Outline every leukocyte.
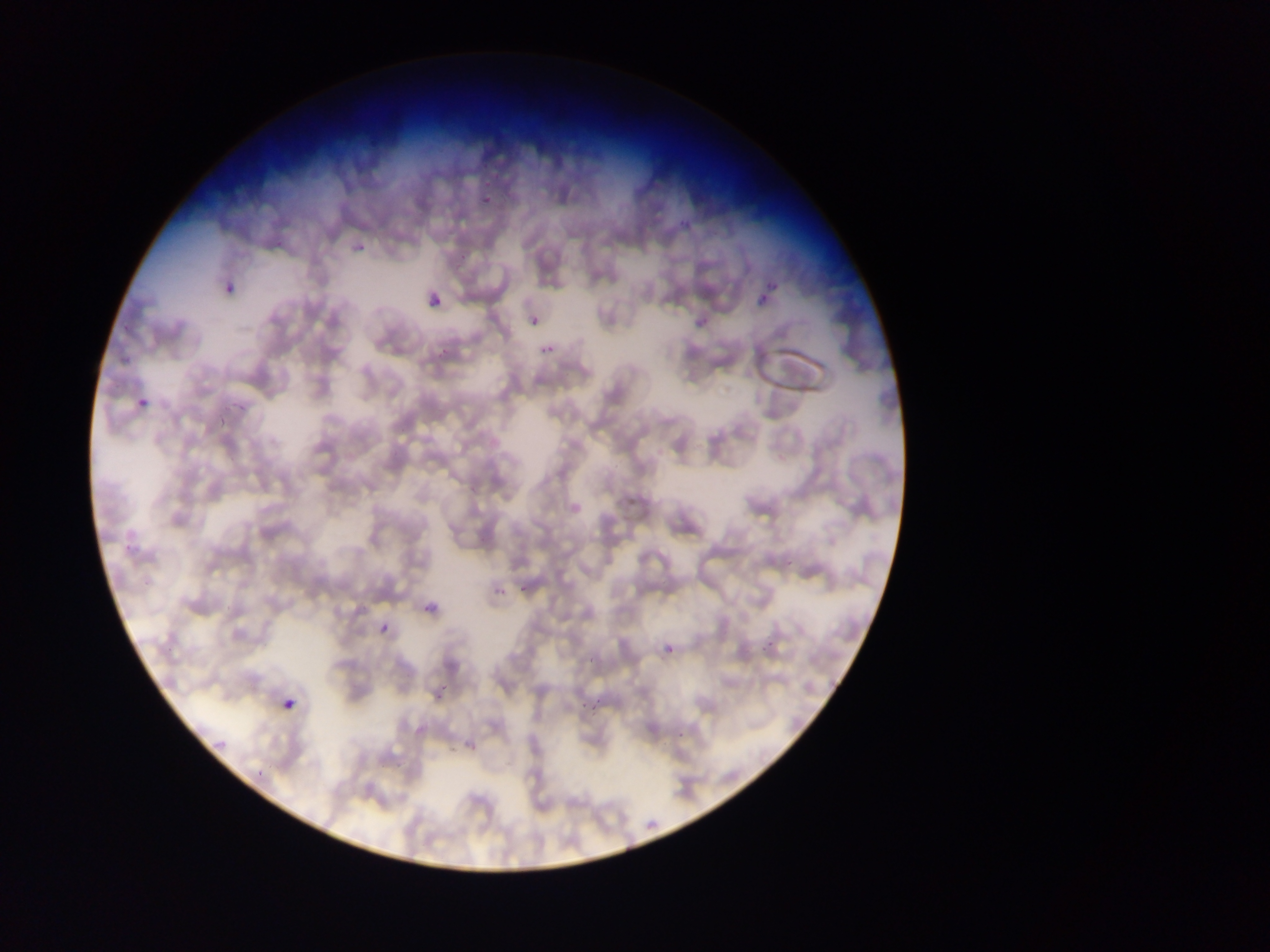

No leukocytes observed.

Approximate bounding boxes as {left, top, right, bottom} in pixels. Malaria parasite locations: {481, 152, 500, 169}, {478, 190, 499, 208}, {674, 214, 694, 227}, {351, 238, 370, 261}, {455, 250, 472, 260}, {754, 268, 783, 293}, {220, 282, 234, 299}, {422, 288, 448, 318}, {755, 295, 768, 305}, {527, 313, 543, 330}, {692, 313, 711, 334}, {539, 340, 557, 359}, {135, 381, 161, 410}, {231, 401, 250, 420}, {214, 414, 228, 428}, {123, 542, 137, 550}, {786, 556, 798, 565}, {521, 580, 530, 592}, {493, 584, 508, 595}, {418, 595, 444, 623}, {374, 620, 394, 637}, {759, 638, 780, 656}, {661, 639, 680, 661}, {591, 656, 599, 666}, {434, 689, 447, 701}, {279, 693, 302, 719}, {592, 701, 602, 715}, {448, 724, 472, 757}, {676, 725, 695, 740}, {393, 753, 414, 775}, {256, 762, 273, 779} | approximate {x, y} pixel centers of objects too small to bound: {580, 708}. Sample from Ghana. One field of view. Thin blood smear. Image is 1270×952 pixels. Mobile-phone photograph taken through the microscope.